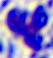

A leukocyte is seen. 400x magnification. Micrograph.